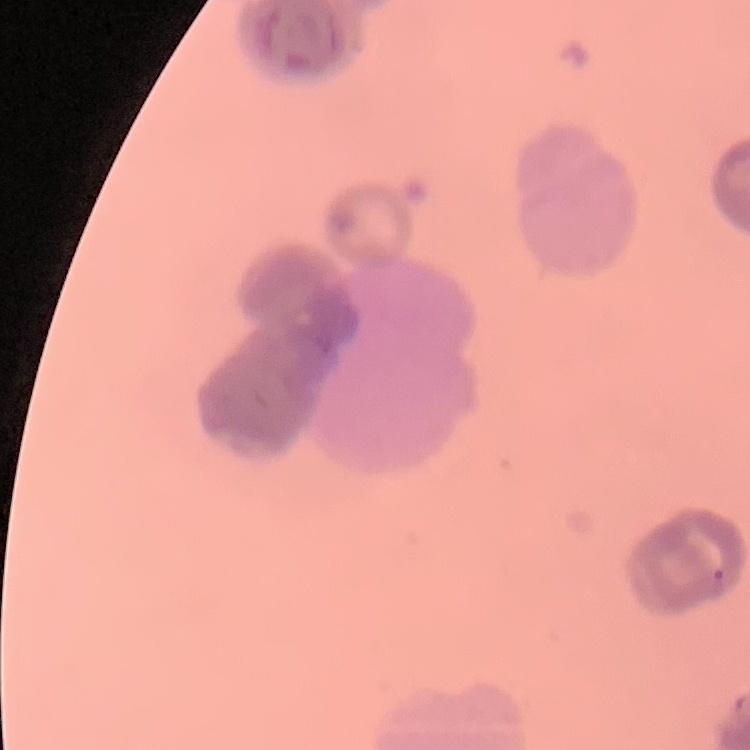
The erythrocytes exhibit rouleaux formation. One tile cut from a larger photomicrograph. Thin blood film. Field's or Giemsa stain.